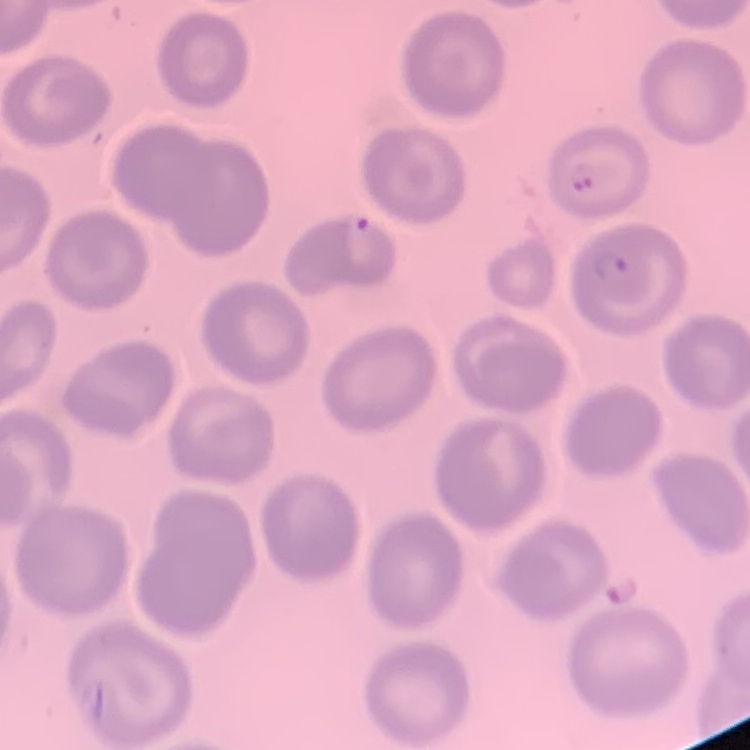
erythrocyte morphology = no rouleaux formation
stain = Field's or Giemsa
preparation = thin blood film
image type = square crop of a larger photomicrograph